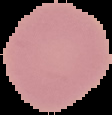
image type = cell region segmented out of the field of view; surrounding area masked to black
image size = 112×115 pixels
preparation = thin blood smear
malaria status = uninfected